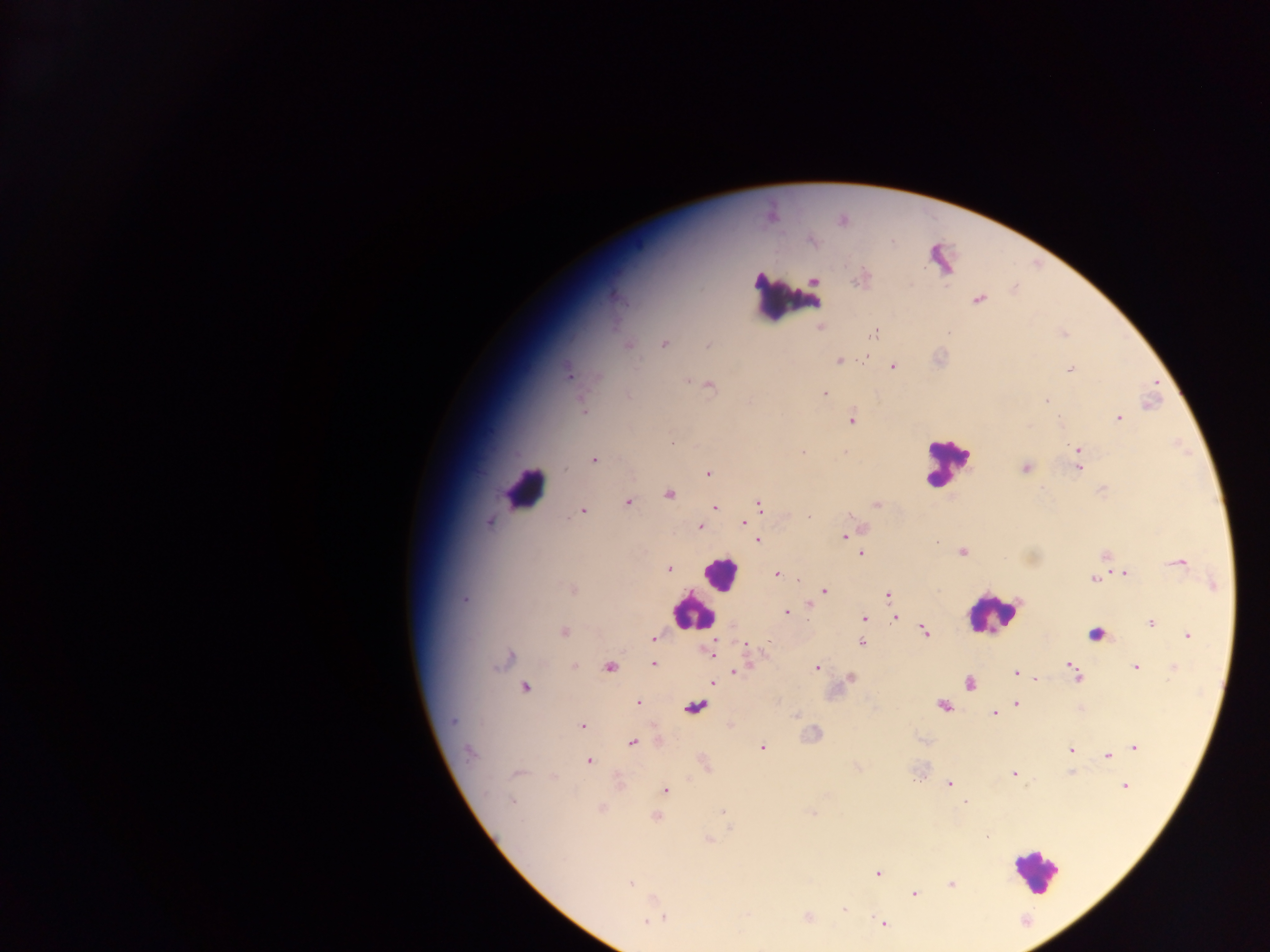
Approximate centers as (x, y) in pixels. Malaria parasite locations: (843, 221), (812, 241), (861, 278), (757, 279), (815, 280), (979, 300), (820, 326), (874, 334), (664, 343), (708, 345), (628, 346), (839, 361), (892, 366), (1071, 369), (568, 373), (687, 381), (711, 386), (825, 394), (628, 396), (1047, 402), (584, 411), (1118, 418), (852, 420), (673, 443), (1077, 449), (803, 452), (844, 452), (594, 460), (1025, 468), (1079, 468), (709, 474), (669, 494), (628, 502), (760, 505), (876, 505), (715, 507), (582, 511), (809, 516), (490, 522), (744, 524), (699, 526), (861, 529), (844, 537), (758, 540), (937, 542), (963, 552), (861, 554), (1105, 556), (1176, 562), (668, 569), (1124, 573), (777, 574), (1093, 579), (572, 589), (824, 591), (889, 596), (465, 600), (786, 612), (896, 618), (865, 619), (1151, 623), (563, 632), (924, 632), (1188, 636), (654, 638), (861, 643), (745, 644), (709, 651), (508, 658), (502, 661), (653, 664), (1070, 665), (574, 666), (816, 667), (1136, 667), (609, 668), (1174, 669), (737, 671), (1016, 673), (1076, 677), (851, 678), (1036, 679), (713, 682), (970, 684), (526, 687), (638, 703), (1017, 704), (943, 705), (695, 707), (993, 714), (796, 715), (453, 722), (582, 726), (632, 742), (763, 747), (1135, 747), (1070, 750), (469, 753), (1107, 756), (589, 761), (517, 773), (1013, 773), (949, 783), (1125, 786), (665, 790), (513, 801), (966, 802), (601, 808), (723, 811), (811, 813), (656, 816), (731, 828), (709, 840), (877, 873), (629, 883), (951, 884), (914, 894), (844, 910), (747, 913), (808, 916), (646, 921), (882, 923). Leukocyte locations: (789, 300), (947, 462), (524, 489), (719, 573), (692, 611), (991, 615), (1097, 633), (1035, 871). Single field of view. Image is 1270×952 pixels. Sample from Ghana. Thick blood film. Mobile-phone photograph taken through the microscope.